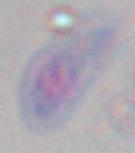

Summary:
  - Modality: photomicrograph
  - Magnification: 1000x
  - Identification: Toxoplasma gondii